Assess this cell for malaria.
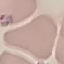
Parasitized.

Summary:
  - Preparation: thin blood film
  - Capture: smartphone camera at the microscope eyepiece
  - Stain: Giemsa
  - Image type: automatically extracted cell patch, resized to 64 × 64 pixels